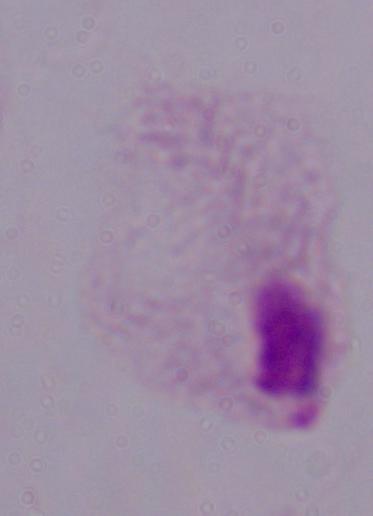

1000x magnification. Micrograph. A trichomonad is seen.